Describe the morphology of the red blood cells.
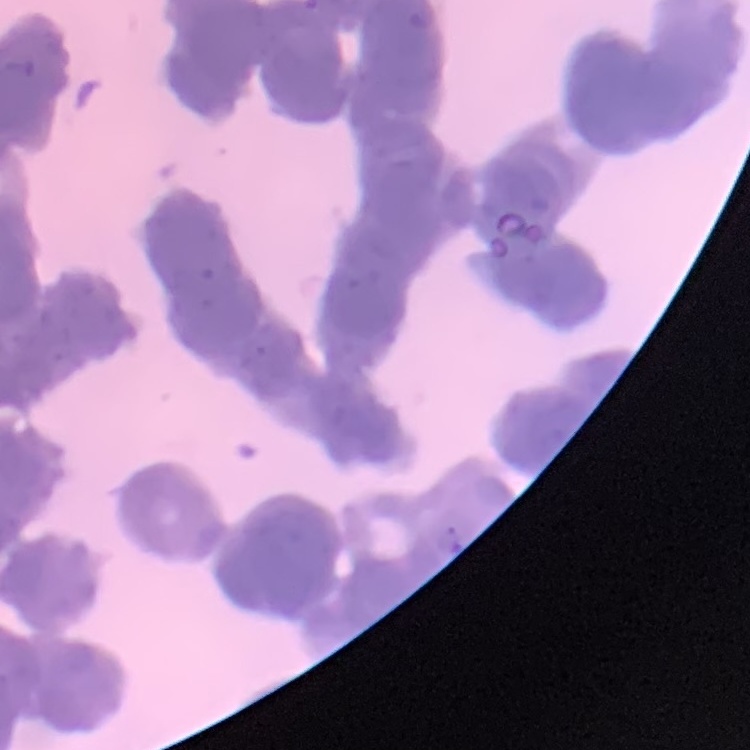

Rouleaux formation.

stain = Field's or Giemsa
preparation = thin peripheral smear
image type = square crop of a larger photomicrograph